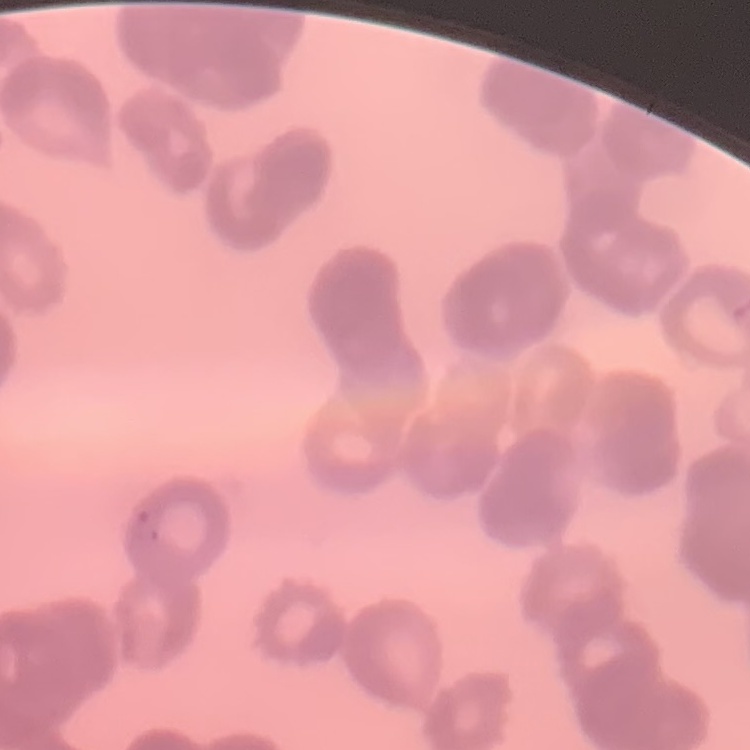 The red blood cells show rouleaux formation. Thin blood film. Square crop of a larger photomicrograph. Stained with either Field's or Giemsa.